Point out every Plasmodium parasite.
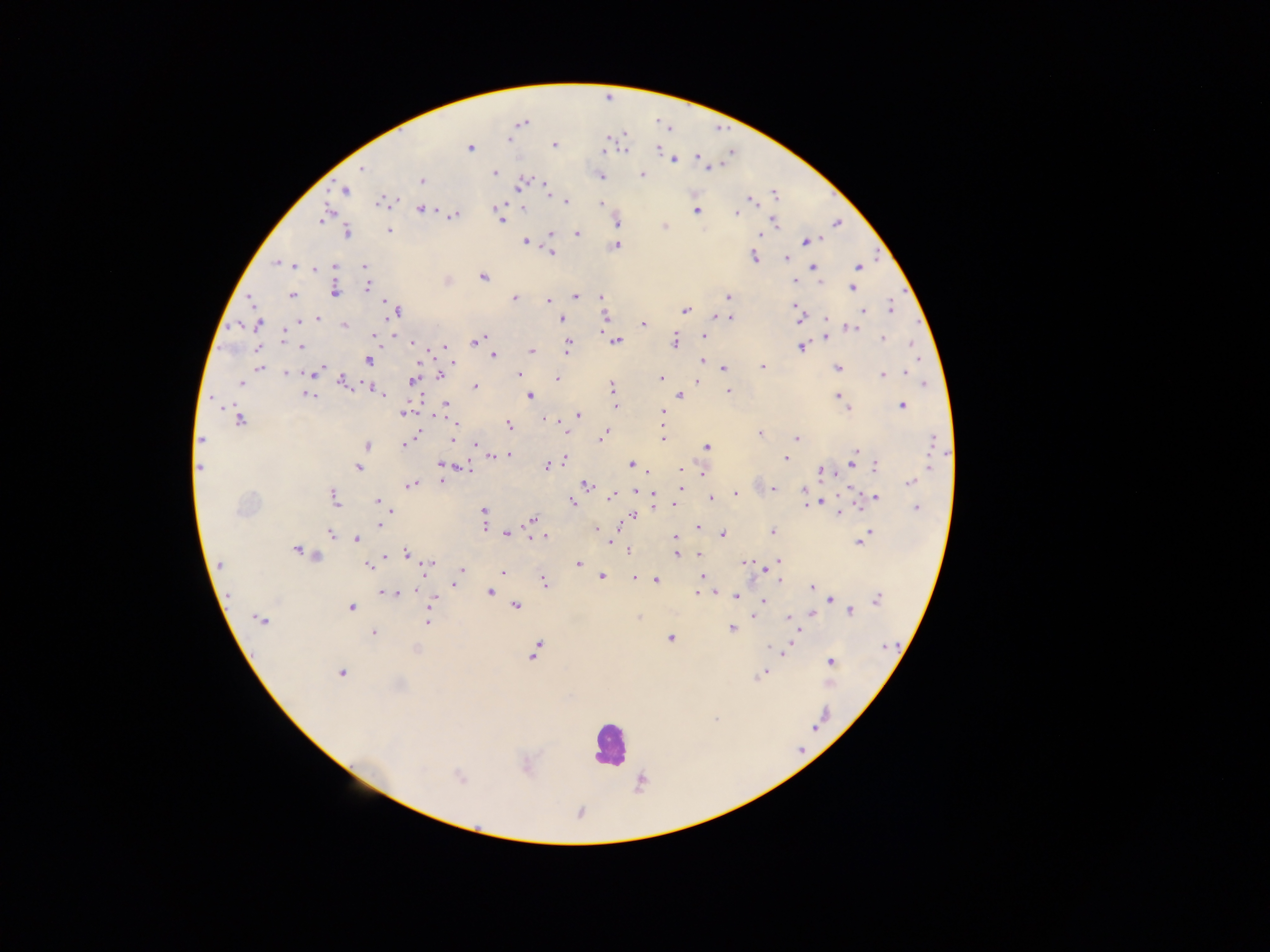

Approximate centers as {x, y} in pixels.
Plasmodium parasites: {509, 140}, {555, 145}, {470, 147}, {625, 149}, {658, 149}, {604, 151}, {696, 157}, {674, 160}, {362, 167}, {712, 167}, {495, 173}, {642, 175}, {601, 176}, {421, 181}, {521, 184}, {546, 189}, {345, 190}, {775, 194}, {751, 200}, {566, 201}, {381, 202}, {600, 203}, {503, 205}, {523, 207}, {420, 209}, {696, 210}, {736, 213}, {455, 215}, {322, 219}, {501, 220}, {774, 222}, {618, 223}, {838, 223}, {664, 226}, {389, 230}, {347, 232}, {552, 234}, {577, 234}, {760, 235}, {807, 240}, {526, 242}, {616, 245}, {553, 252}, {753, 256}, {786, 258}, {275, 263}, {294, 266}, {335, 266}, {364, 267}, {858, 267}, {813, 268}, {313, 269}, {482, 277}, {796, 282}, {367, 286}, {851, 287}, {335, 292}, {292, 295}, {575, 297}, {601, 297}, {727, 297}, {514, 299}, {250, 300}, {549, 300}, {388, 305}, {795, 306}, {891, 308}, {397, 310}, {685, 310}, {863, 310}, {715, 315}, {605, 316}, {561, 318}, {827, 318}, {317, 319}, {731, 319}, {798, 320}, {258, 323}, {643, 323}, {344, 326}, {851, 328}, {375, 334}, {283, 335}, {704, 336}, {826, 337}, {883, 338}, {285, 339}, {616, 340}, {475, 341}, {674, 341}, {412, 342}, {913, 345}, {444, 346}, {300, 347}, {568, 347}, {801, 348}, {532, 350}, {493, 355}, {369, 361}, {702, 361}, {259, 368}, {321, 368}, {763, 368}, {837, 368}, {723, 369}, {286, 373}, {315, 373}, {905, 373}, {882, 374}, {440, 375}, {519, 375}, {557, 379}, {661, 379}, {341, 381}, {412, 381}, {698, 381}, {240, 383}, {926, 383}, {612, 385}, {475, 386}, {376, 391}, {729, 391}, {381, 394}, {681, 395}, {308, 396}, {530, 396}, {837, 396}, {212, 398}, {446, 404}, {843, 404}, {615, 406}, {902, 406}, {846, 408}, {663, 411}, {405, 413}, {578, 415}, {240, 420}, {454, 423}, {509, 425}, {567, 433}, {759, 434}, {415, 435}, {603, 435}, {662, 438}, {796, 438}, {201, 440}, {453, 441}, {932, 442}, {404, 444}, {366, 445}, {474, 445}, {706, 446}, {855, 451}, {508, 455}, {499, 456}, {785, 458}, {565, 459}, {853, 462}, {631, 463}, {441, 464}, {548, 466}, {875, 466}, {929, 466}, {199, 468}, {358, 468}, {680, 470}, {824, 472}, {703, 473}, {441, 481}, {910, 482}, {412, 484}, {586, 484}, {680, 489}, {774, 489}, {636, 491}, {804, 491}, {654, 493}, {735, 494}, {612, 495}, {334, 497}, {710, 498}, {876, 498}, {377, 500}, {572, 503}, {820, 503}, {806, 504}, {672, 505}, {916, 508}, {483, 511}, {840, 513}, {633, 516}, {533, 520}, {379, 525}, {485, 526}, {697, 527}, {598, 529}, {773, 532}, {869, 532}, {331, 533}, {506, 533}, {723, 535}, {543, 537}, {676, 538}, {356, 539}, {609, 541}, {860, 542}, {297, 549}, {629, 551}, {407, 554}, {699, 554}, {677, 555}, {385, 556}, {316, 557}, {745, 561}, {779, 561}, {578, 564}, {221, 565}, {367, 565}, {429, 565}, {462, 569}, {502, 573}, {701, 576}, {602, 577}, {635, 578}, {655, 580}, {779, 580}, {544, 582}, {455, 584}, {812, 587}, {385, 592}, {698, 592}, {490, 593}, {397, 594}, {229, 596}, {736, 596}, {877, 599}, {433, 600}, {763, 600}, {830, 600}, {515, 607}, {351, 608}, {850, 612}, {814, 614}, {755, 616}, {638, 618}, {789, 618}, {261, 620}, {428, 622}, {732, 629}, {374, 633}, {670, 638}, {792, 644}, {885, 646}, {773, 649}, {416, 650}, {535, 650}, {786, 650}, {830, 661}, {341, 673}, {762, 674}, {759, 676}, {715, 720}, {458, 776}.

leukocyte locations = approximate centers as {x, y} in pixels: {609, 743}
capture = mobile-phone photograph through a microscope
image size = 1270×952 pixels
country = Ghana
field of view = single
preparation = thick blood smear